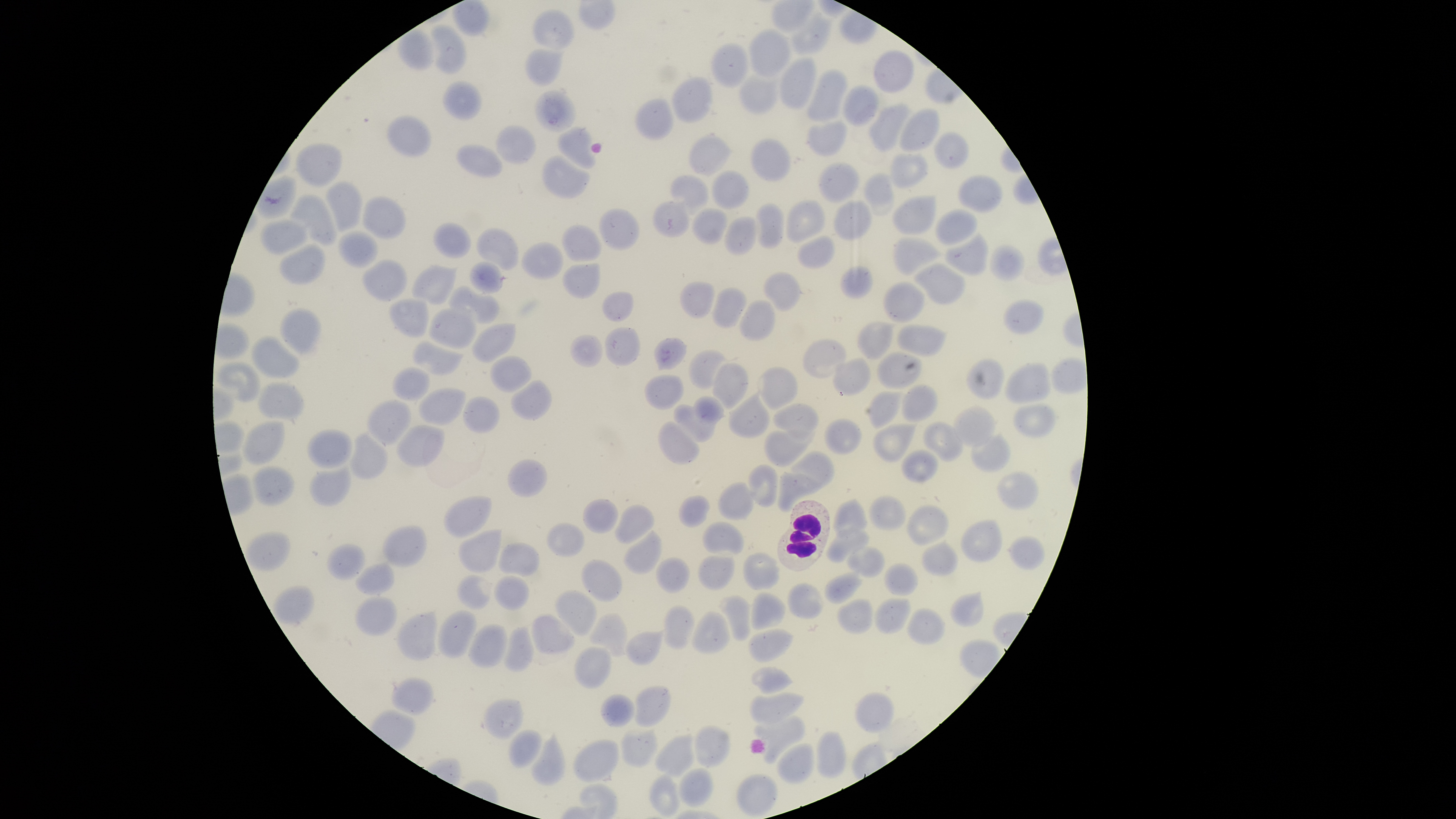
Approximate bounding boxes as [left, top, right, bottom] in pixels. Uninfected RBCs: [533, 8, 575, 51], [790, 9, 834, 54], [432, 23, 468, 75], [398, 27, 435, 71], [748, 28, 792, 78], [711, 42, 748, 89], [525, 48, 565, 86], [873, 50, 914, 93], [779, 57, 816, 109], [806, 69, 848, 122], [738, 75, 779, 115], [672, 77, 713, 123], [442, 81, 481, 121], [842, 84, 879, 127], [534, 88, 576, 134], [634, 97, 673, 142], [868, 102, 912, 152], [899, 109, 941, 152], [386, 114, 432, 158], [806, 121, 847, 157], [495, 124, 537, 164], [556, 126, 596, 170], [933, 131, 970, 170], [689, 134, 732, 176], [751, 138, 791, 181], [296, 142, 342, 187], [456, 145, 503, 178], [889, 152, 929, 189], [543, 153, 590, 199], [817, 161, 860, 203], [710, 169, 749, 209], [863, 172, 895, 216], [257, 173, 297, 219], [670, 174, 709, 215], [956, 174, 1004, 213], [325, 180, 362, 233], [289, 192, 337, 246], [362, 195, 406, 240], [892, 195, 937, 236], [786, 199, 826, 245], [652, 200, 690, 237], [755, 201, 785, 249], [833, 201, 872, 240], [597, 207, 639, 250], [692, 207, 728, 244], [934, 209, 979, 245], [723, 215, 757, 256], [260, 218, 308, 256], [433, 222, 472, 258], [560, 223, 602, 262], [477, 227, 519, 271], [337, 230, 378, 269], [944, 231, 989, 276], [797, 235, 835, 269], [892, 237, 943, 277], [521, 241, 564, 280], [278, 243, 326, 285], [989, 245, 1025, 281], [361, 259, 407, 302], [468, 260, 504, 293], [562, 262, 600, 299], [912, 262, 967, 304], [410, 264, 459, 305], [840, 266, 874, 300], [763, 271, 804, 311], [679, 279, 716, 319], [883, 281, 925, 323], [448, 285, 500, 323], [711, 286, 748, 329], [601, 291, 633, 322], [387, 297, 430, 339], [738, 298, 776, 342], [1002, 298, 1045, 334], [278, 306, 322, 355], [428, 306, 476, 350], [857, 321, 896, 360], [471, 322, 517, 363], [896, 324, 946, 357], [604, 326, 641, 367], [569, 333, 603, 367], [251, 335, 300, 379], [654, 337, 688, 371], [802, 337, 847, 378], [411, 340, 465, 376], [689, 349, 728, 389], [876, 351, 923, 389], [489, 356, 532, 394], [832, 357, 870, 397], [965, 358, 1005, 400], [214, 361, 261, 402], [1004, 361, 1051, 404], [712, 362, 748, 410], [391, 366, 429, 403], [758, 367, 797, 411], [643, 374, 683, 410], [510, 379, 552, 420], [257, 381, 304, 420], [902, 383, 938, 422], [418, 387, 467, 426], [728, 389, 770, 439], [868, 390, 903, 429], [693, 395, 724, 425], [463, 396, 501, 434], [366, 398, 411, 447], [771, 402, 820, 444], [1012, 403, 1057, 437], [673, 404, 715, 443], [953, 405, 997, 447], [824, 418, 862, 454], [242, 420, 285, 466], [657, 420, 699, 465], [923, 421, 963, 461], [872, 422, 918, 462], [396, 424, 445, 468], [307, 429, 352, 468], [763, 429, 816, 466], [348, 431, 389, 479], [970, 431, 1010, 472], [901, 449, 938, 482], [791, 450, 835, 488], [508, 461, 545, 497], [309, 464, 352, 508], [747, 464, 779, 508], [252, 466, 295, 505], [777, 470, 824, 512], [996, 472, 1039, 510], [717, 482, 757, 521], [868, 494, 906, 530], [443, 495, 492, 539], [678, 495, 711, 527], [582, 498, 619, 534], [832, 498, 866, 537], [613, 503, 655, 544], [905, 504, 949, 546], [960, 518, 1003, 562], [702, 520, 744, 556], [546, 522, 585, 557], [382, 526, 427, 569], [826, 527, 869, 562], [623, 528, 662, 574], [459, 529, 503, 573], [1005, 535, 1046, 570], [921, 539, 959, 576], [325, 542, 365, 581], [498, 542, 539, 578], [846, 546, 886, 576], [743, 552, 781, 591], [697, 555, 735, 591], [655, 556, 690, 594], [580, 558, 622, 603], [354, 562, 396, 595], [884, 562, 918, 596], [824, 569, 864, 605], [456, 574, 496, 610], [494, 575, 530, 610], [787, 582, 825, 620], [554, 589, 597, 636], [751, 591, 786, 630], [949, 591, 985, 628], [355, 595, 398, 638], [717, 595, 751, 641], [836, 597, 872, 634], [873, 598, 912, 634], [663, 605, 695, 651], [906, 607, 945, 644], [436, 610, 477, 658], [691, 610, 732, 655], [396, 611, 437, 661], [589, 613, 629, 657], [531, 614, 576, 655], [467, 623, 508, 668], [504, 627, 535, 672], [626, 627, 667, 666], [748, 627, 794, 662], [573, 645, 612, 689], [750, 666, 794, 694], [390, 676, 434, 715], [634, 685, 670, 727], [749, 691, 804, 724], [853, 691, 895, 734], [600, 693, 634, 728], [484, 698, 524, 740], [753, 714, 806, 765], [694, 724, 729, 768], [507, 728, 542, 768], [620, 729, 658, 768], [529, 731, 567, 786], [815, 731, 846, 778], [654, 733, 695, 778], [572, 739, 619, 783], [776, 743, 814, 785], [678, 768, 714, 807], [649, 772, 680, 817], [736, 772, 778, 817]. WBCs: [777, 499, 831, 572]. One field of view of the specimen. Smartphone photograph through the microscope eyepiece. Giemsa stain. Image is 1456×819 pixels. Thin blood film. Presence: no malaria parasites identified. Circular visible region.